Give the position of every Plasmodium parasite visible.
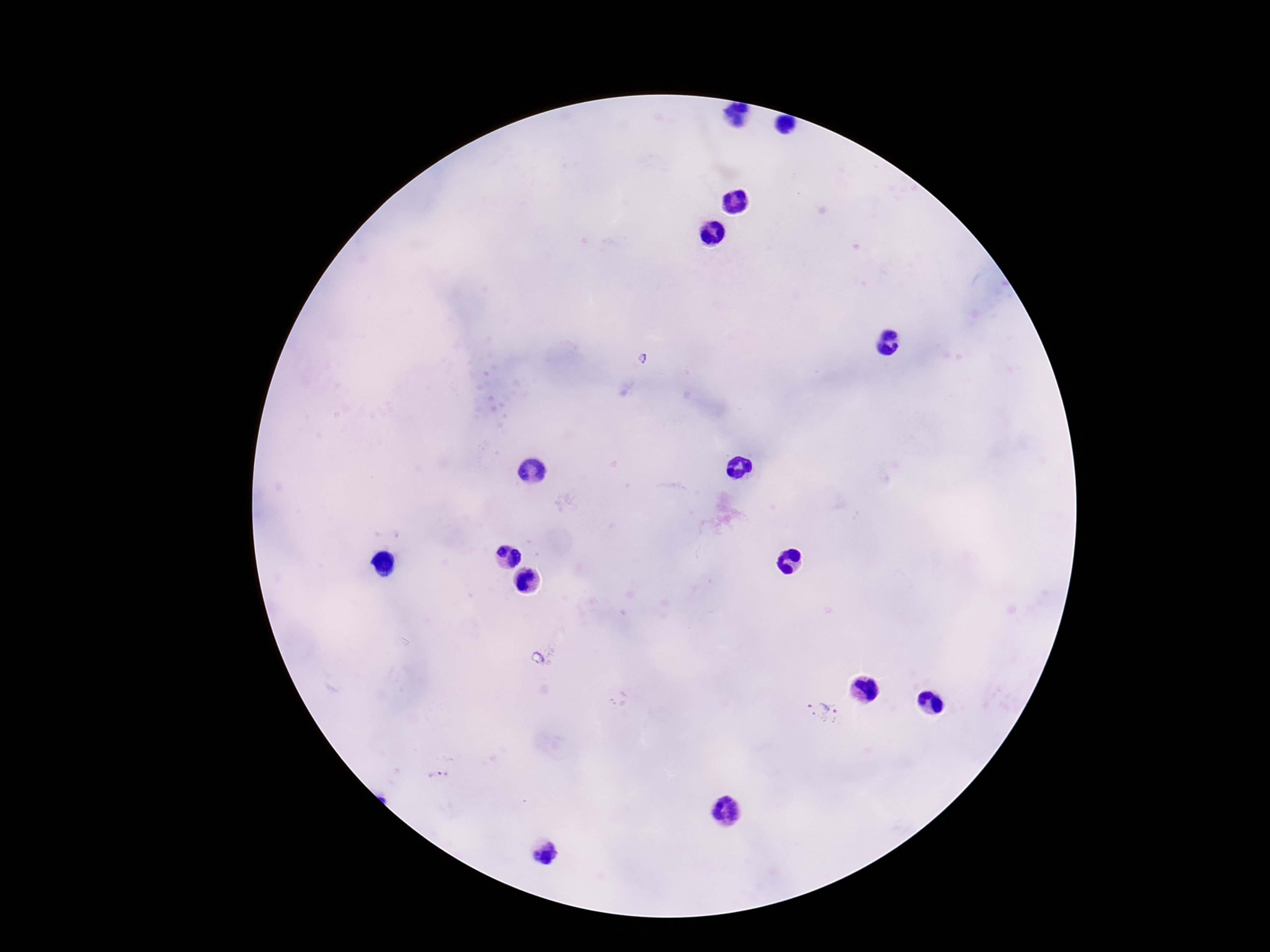

Approximate centers as (x, y) in pixels.
Plasmodium parasites: (643, 358), (824, 711), (437, 779).

Image is 1270×952 pixels. 100x magnification. Thick blood film. Patient malaria status: positive. Giemsa-stained preparation. Photographed through the microscope eyepiece with a smartphone camera. One field from this slide.